Point out Plasmodium parasites and leukocytes.
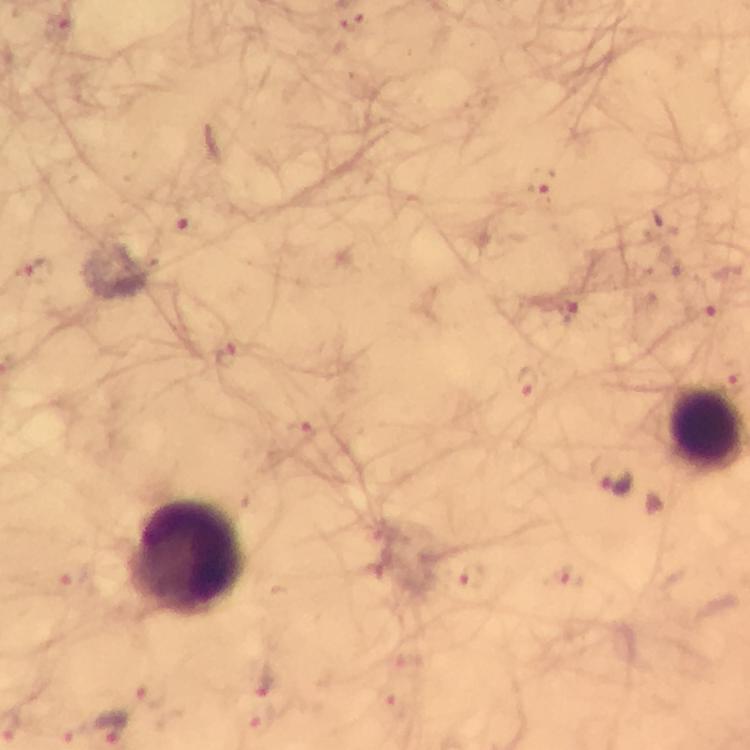

Approximate object centers, in pixels from the top-left corner.
Plasmodium parasites: (x=62, y=29), (x=542, y=183), (x=188, y=229), (x=667, y=270), (x=32, y=272), (x=567, y=311), (x=707, y=312), (x=229, y=354), (x=529, y=383), (x=298, y=435), (x=616, y=481), (x=569, y=577), (x=73, y=580), (x=473, y=583), (x=268, y=684), (x=151, y=691), (x=108, y=724), (x=69, y=729).
Leukocytes: (x=191, y=560).

Image is 750×750 pixels. Photographed with a smartphone mounted on the microscope. From a diagnostic examination for malaria. Thick blood smear. At 100x magnification. Giemsa stain. Immersion oil was used. A crop from one field of view.